Look for parasitized red blood cells.
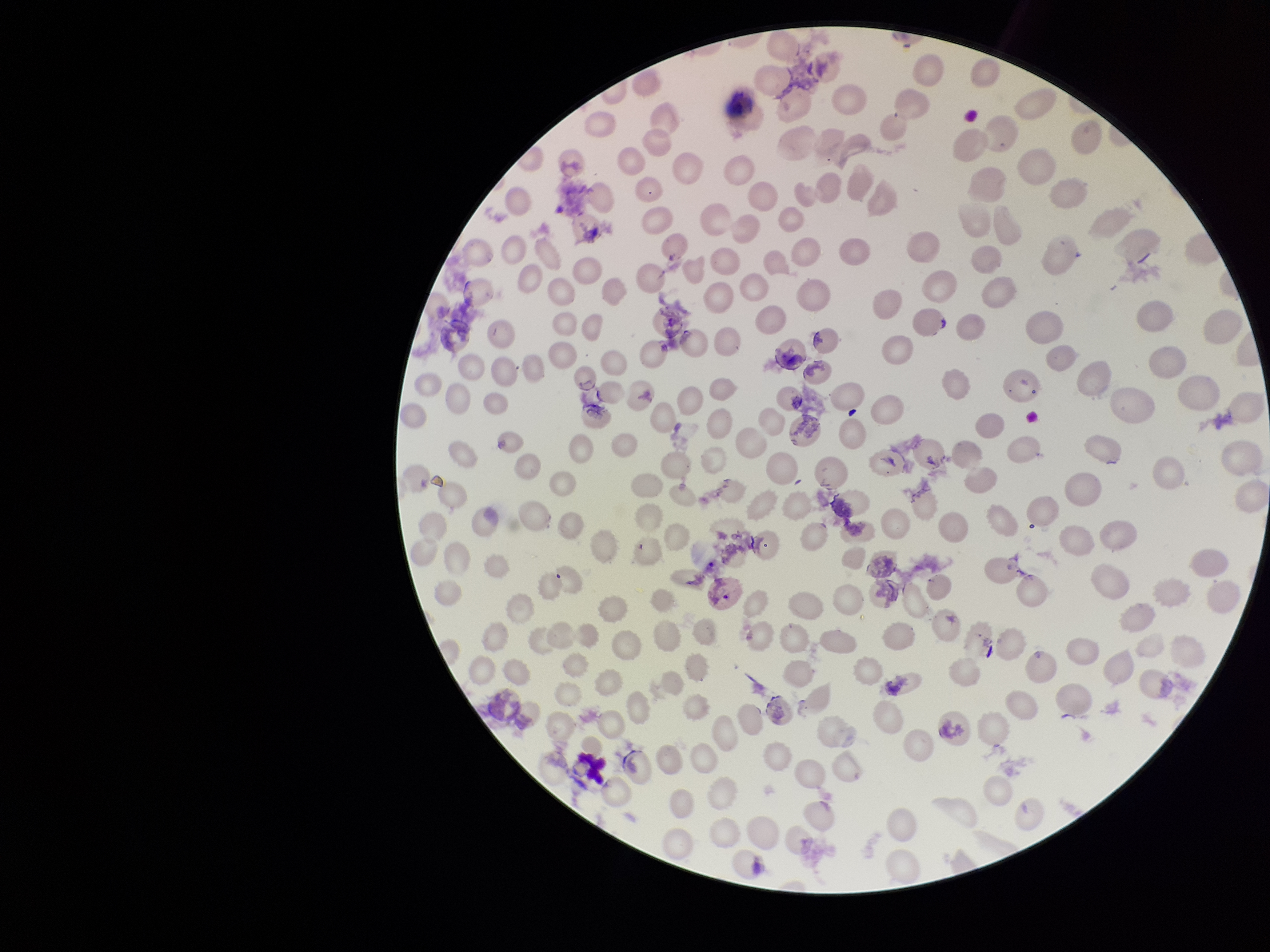
None seen.

parasitized red blood cell count = 0
stain = Giemsa
species reported for this patient = Plasmodium vivax
red blood cell count = 224
preparation = thin blood smear
capture = smartphone photograph through the microscope eyepiece
field of view = single
patient malaria status = positive
image size = 1270×952 pixels